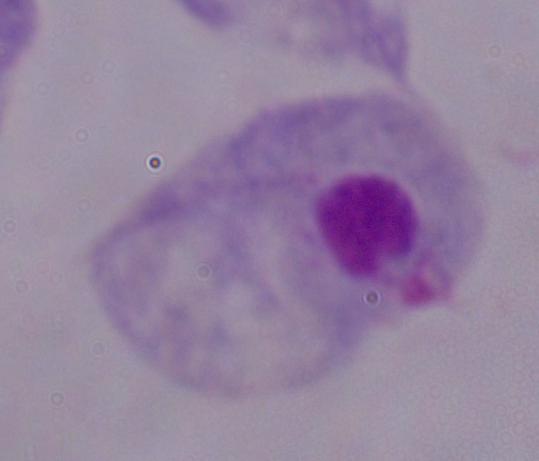
Micrograph. A trichomonad is shown. 1000x magnification.